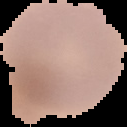
Segmented cell region on a black background. From a thin blood smear. Result: Plasmodium parasites detected. Image is 127×127 pixels.